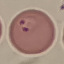
Summary:
  - Result: malaria parasites detected
  - Preparation: thin blood film
  - Stain: Giemsa
  - Capture: smartphone through the microscope eyepiece
  - Image type: cell patch, automatically extracted from a larger field of view and resized to 64 × 64 pixels